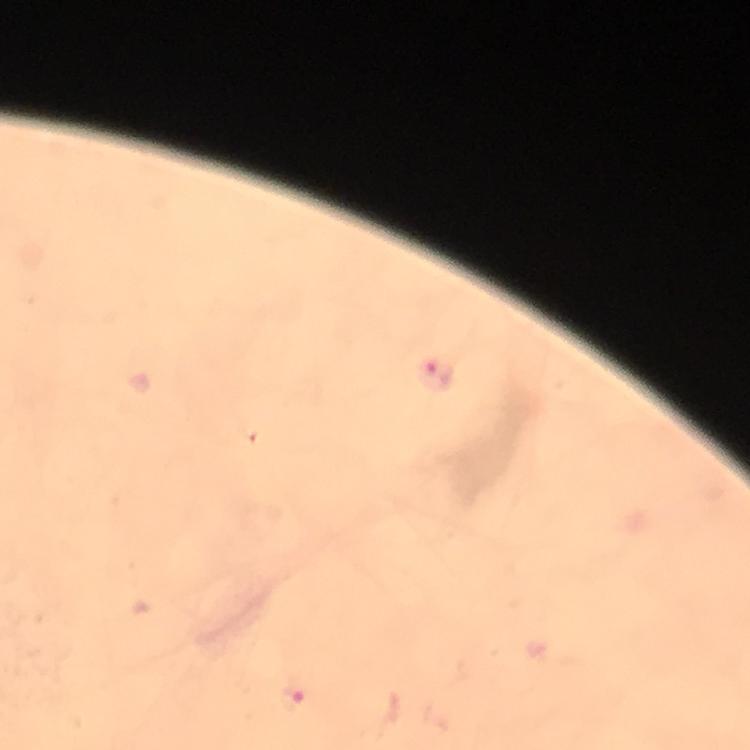
Approximate centers as (x, y) in pixels. Malaria parasite locations: (438, 374), (292, 701). At 100x magnification. Photographed through the microscope with a smartphone camera. Giemsa-stained preparation. A crop from one field of view. Immersion oil applied. Image is 750×750 pixels. From a malaria diagnostic workup. Thick smear.